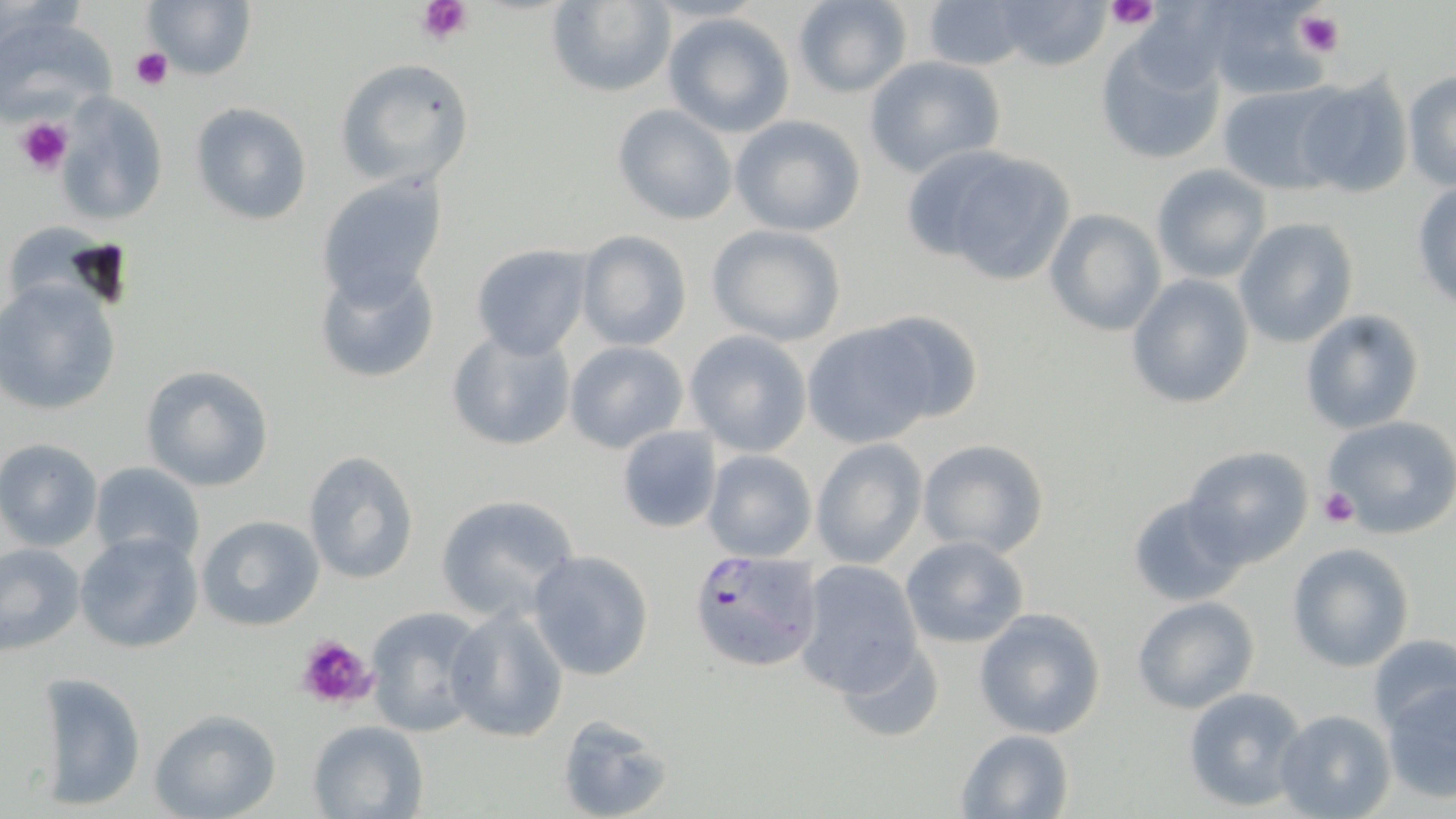 Approximate bounding boxes as (x1,y1)-(x2,y2) corner pairs in pixels. Uninfected red blood cell locations: (142,0)-(257,82), (543,0)-(677,98), (789,0)-(913,97), (991,0)-(1116,71), (918,1)-(1038,71), (1197,2)-(1327,99), (662,10)-(797,137), (0,11)-(116,123), (1095,39)-(1226,166), (865,56)-(1006,178), (333,58)-(475,187), (1404,69)-(1456,191), (1292,75)-(1413,199), (1216,82)-(1342,194), (56,95)-(168,225), (189,103)-(313,225), (611,103)-(739,225), (728,115)-(867,237), (915,146)-(1080,287), (1151,163)-(1273,284), (318,172)-(449,307), (1411,181)-(1456,308), (1044,208)-(1165,337), (12,216)-(106,316), (1233,218)-(1358,348), (706,223)-(846,345), (575,231)-(693,352), (470,244)-(592,358), (311,259)-(443,385), (1126,273)-(1255,410), (0,279)-(124,418), (862,308)-(987,427), (1300,310)-(1425,434), (801,318)-(932,446), (445,325)-(577,453), (684,330)-(812,457), (564,340)-(689,453), (138,365)-(273,493), (1323,415)-(1456,538), (617,424)-(721,534), (916,437)-(1049,559), (0,438)-(103,551), (810,438)-(926,569), (1182,446)-(1313,566), (701,450)-(816,562), (300,451)-(420,585), (89,460)-(205,566), (1127,492)-(1251,607), (434,494)-(579,624), (196,515)-(325,633), (74,529)-(204,655), (900,535)-(1029,648), (0,541)-(86,656), (1286,542)-(1414,671), (527,550)-(655,680), (792,560)-(925,697), (1131,596)-(1259,715), (363,606)-(488,738), (975,607)-(1107,740), (444,608)-(570,743), (1366,633)-(1456,736), (835,636)-(943,745), (35,670)-(146,810), (1380,679)-(1456,804), (1181,685)-(1308,812), (148,708)-(281,819), (1274,709)-(1396,819), (554,714)-(676,819), (305,719)-(430,818), (955,728)-(1076,819). Plasmodium falciparum-infected red blood cell locations: (686,546)-(824,674). Platelet locations: (415,0)-(475,43), (1106,0)-(1160,30), (1294,9)-(1345,57), (131,48)-(173,91), (16,117)-(72,174), (1319,487)-(1360,529), (292,632)-(379,713). Slide-level diagnosis: Plasmodium falciparum. One field of a larger specimen. Thin blood film. Image is 1456×819 pixels. Captured at 1000x magnification. Light microscopy. May-Grünwald-Giemsa-stained preparation.